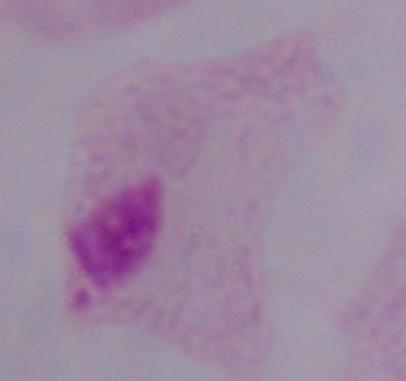

A trichomonad is seen. Photomicrograph. Captured at 1000x magnification.